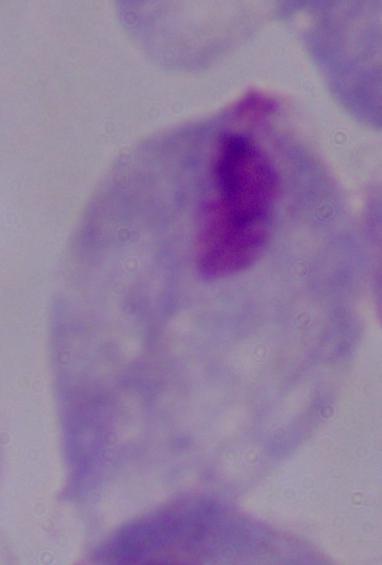 A trichomonad is seen. Photomicrograph. 1000x magnification.